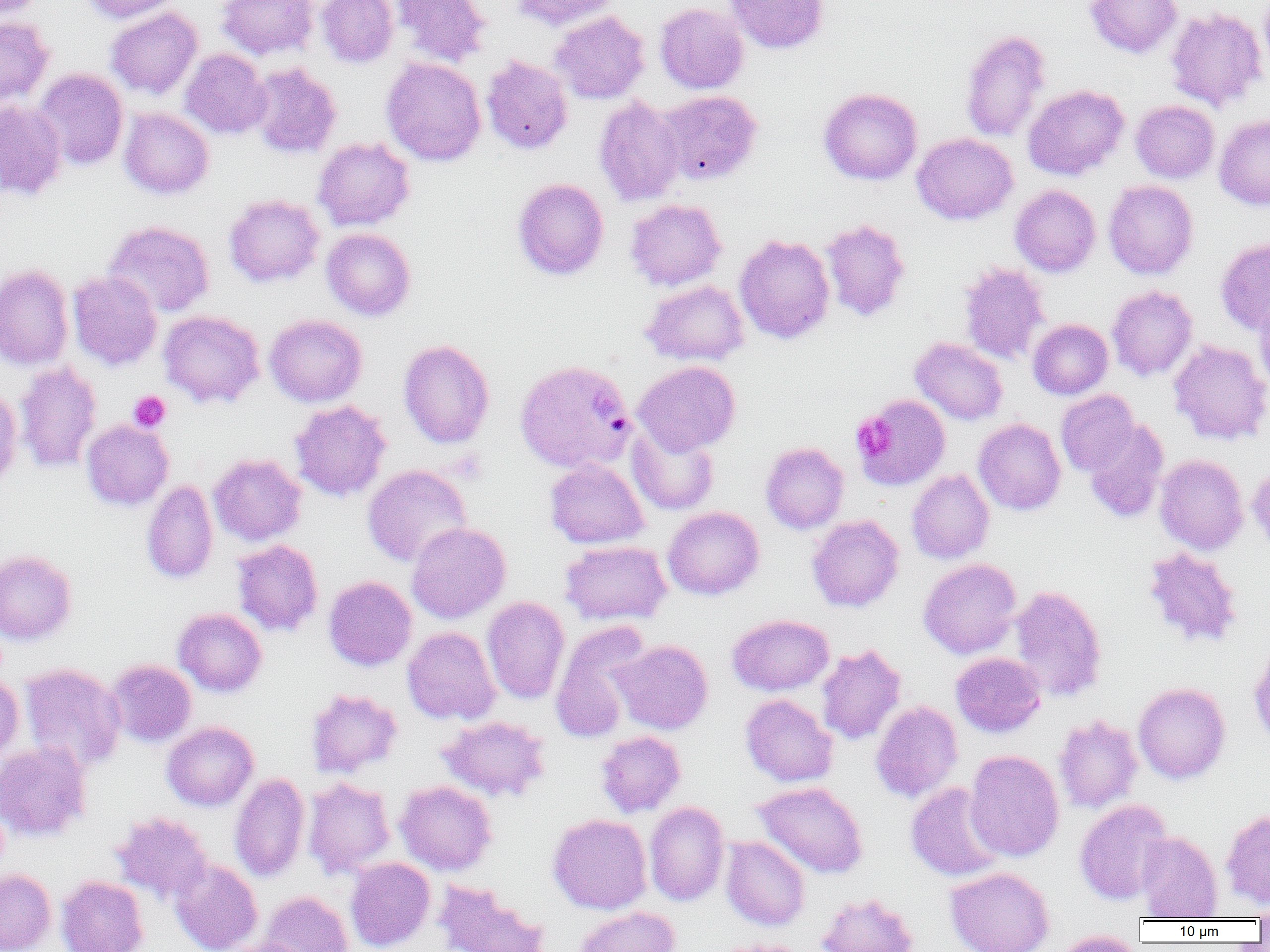
Summary:
  - Coordinate format: approximate bounding boxes as [x1, y1, x2, y2] in pixels
  - Platelet locations: [128, 391, 171, 432], [851, 413, 897, 460]
  - Plasmodium vivax-infected red blood cell locations: [515, 358, 636, 473]
  - Uninfected red blood cell locations: [1, 0, 44, 20], [81, 0, 183, 23], [217, 0, 319, 60], [316, 0, 399, 68], [391, 0, 492, 68], [509, 0, 619, 30], [723, 0, 829, 54], [1085, 0, 1182, 58], [654, 2, 749, 94], [106, 7, 203, 99], [1165, 7, 1268, 112], [550, 11, 650, 104], [0, 17, 54, 109], [960, 29, 1051, 142], [180, 48, 272, 139], [481, 56, 573, 155], [381, 57, 487, 166], [248, 63, 342, 158], [33, 69, 128, 171], [1023, 84, 1129, 180], [819, 87, 922, 185], [657, 90, 762, 186], [593, 96, 685, 207], [1131, 100, 1220, 184], [0, 101, 67, 200], [119, 108, 214, 199], [1214, 115, 1270, 210], [912, 133, 1018, 225], [313, 138, 415, 231], [512, 178, 609, 280], [1103, 180, 1199, 279], [1010, 184, 1101, 277], [224, 194, 325, 287], [625, 199, 727, 291], [820, 218, 911, 323], [103, 221, 215, 317], [322, 228, 416, 320], [734, 234, 835, 344], [1215, 237, 1270, 335], [960, 263, 1050, 364], [0, 264, 73, 370], [67, 271, 162, 371], [640, 280, 749, 366], [1107, 285, 1198, 381], [1254, 294, 1270, 396], [158, 310, 265, 409], [264, 314, 367, 407], [1028, 319, 1113, 399], [910, 337, 1008, 425], [398, 339, 495, 449], [1168, 339, 1270, 445], [632, 361, 741, 455], [14, 362, 102, 473], [0, 385, 22, 493], [1056, 390, 1140, 477], [853, 394, 950, 491], [289, 400, 392, 502], [973, 418, 1066, 515], [81, 419, 174, 511], [1083, 419, 1169, 522], [626, 423, 720, 516], [760, 442, 849, 534], [208, 453, 307, 546], [1154, 454, 1249, 555], [545, 459, 649, 549], [1248, 463, 1270, 555], [362, 465, 471, 567], [906, 469, 994, 564], [141, 480, 218, 584], [662, 506, 765, 600], [807, 514, 904, 612], [406, 522, 511, 623], [231, 540, 323, 636], [560, 540, 671, 625], [1143, 547, 1243, 648], [0, 550, 77, 645], [918, 558, 1022, 659], [323, 576, 417, 671], [1008, 585, 1108, 702], [482, 596, 570, 704], [173, 608, 267, 697], [727, 614, 834, 696], [550, 619, 652, 742], [402, 626, 501, 725], [612, 639, 713, 735], [1249, 640, 1270, 749], [817, 644, 906, 745], [950, 652, 1046, 738], [106, 659, 197, 747], [20, 663, 126, 773], [0, 673, 24, 766], [1133, 682, 1230, 784], [306, 688, 403, 778], [740, 694, 838, 787], [870, 700, 963, 803], [1053, 714, 1143, 813], [436, 715, 550, 802], [162, 721, 259, 811], [595, 730, 686, 817], [0, 740, 92, 842], [964, 750, 1064, 862], [229, 773, 310, 882], [303, 777, 396, 878], [394, 781, 497, 876], [752, 781, 868, 878], [905, 782, 1005, 882], [1074, 798, 1174, 905], [644, 801, 729, 906], [1221, 807, 1270, 909], [111, 812, 213, 904], [547, 813, 652, 914], [1136, 831, 1222, 920], [721, 836, 810, 931], [345, 857, 435, 952], [169, 859, 263, 952], [945, 866, 1055, 952], [0, 869, 56, 952], [56, 876, 148, 952], [432, 879, 550, 952], [259, 891, 354, 952], [816, 892, 918, 952], [1248, 900, 1270, 924], [573, 906, 679, 952], [1052, 930, 1143, 952], [217, 938, 311, 952], [709, 939, 810, 952]
  - Slide-level diagnosis: Plasmodium vivax
  - Modality: light microscopy
  - Magnification: 1000x
  - Image size: 1270×952 pixels
  - Preparation: thin blood smear
  - Field of view: one of a larger specimen